Name the blood parasite species.
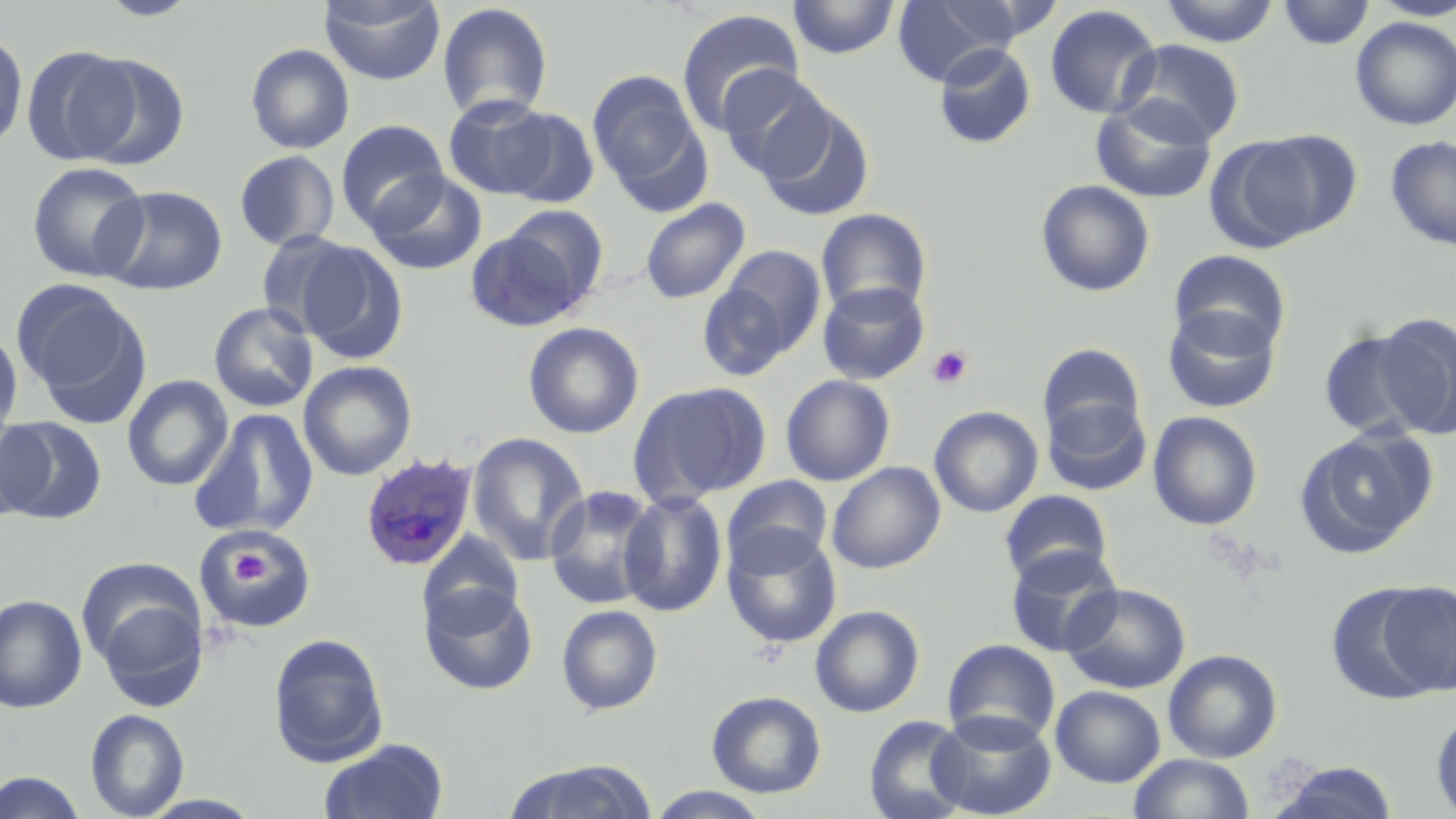

Plasmodium ovale.

Approximate bounding boxes as (x1, y1, x2, y2) in pixels. Platelet locations: (927, 345, 973, 389), (223, 540, 276, 591). Uninfected red blood cell locations: (96, 0, 203, 20), (319, 0, 445, 85), (787, 0, 900, 59), (890, 0, 1019, 87), (1156, 0, 1281, 46), (1275, 0, 1375, 50), (1370, 1, 1456, 21), (436, 2, 554, 122), (1044, 4, 1162, 120), (676, 7, 804, 135), (1351, 16, 1456, 130), (0, 31, 27, 155), (1117, 40, 1245, 145), (933, 42, 1036, 148), (245, 43, 354, 154), (22, 45, 140, 166), (72, 54, 190, 170), (717, 65, 832, 180), (588, 70, 708, 206), (442, 94, 560, 199), (1091, 96, 1217, 203), (757, 101, 874, 222), (498, 108, 599, 208), (336, 119, 449, 233), (1241, 130, 1363, 241), (1385, 134, 1456, 250), (234, 151, 340, 251), (26, 161, 150, 282), (366, 171, 487, 276), (1036, 179, 1156, 297), (98, 185, 228, 295), (640, 198, 751, 304), (500, 204, 610, 310), (815, 208, 932, 316), (465, 228, 588, 332), (254, 230, 358, 338), (297, 241, 409, 363), (716, 245, 826, 359), (1169, 249, 1292, 357), (817, 282, 930, 385), (15, 283, 150, 425), (697, 284, 794, 381), (208, 302, 319, 413), (1163, 306, 1281, 414), (1375, 314, 1456, 439), (523, 321, 644, 439), (0, 327, 23, 447), (1317, 328, 1433, 441), (1037, 343, 1146, 443), (299, 360, 417, 480), (123, 375, 233, 491), (780, 375, 895, 486), (629, 380, 773, 506), (1042, 399, 1151, 496), (929, 406, 1043, 517), (190, 409, 319, 538), (1147, 411, 1263, 530), (0, 416, 107, 524), (0, 417, 48, 524), (1294, 426, 1438, 558), (466, 431, 590, 565), (827, 461, 945, 573), (722, 475, 833, 574), (545, 485, 660, 610), (999, 490, 1113, 586), (619, 491, 727, 617), (194, 524, 317, 633), (722, 527, 842, 649), (418, 531, 524, 634), (1005, 546, 1123, 657), (1375, 581, 1456, 697), (419, 583, 539, 695), (1061, 583, 1191, 694), (89, 584, 210, 712), (0, 594, 87, 713), (556, 604, 662, 715), (810, 605, 925, 717), (268, 633, 389, 767), (943, 639, 1060, 748), (1163, 649, 1282, 763), (1051, 685, 1165, 787), (707, 690, 827, 798), (85, 708, 189, 818), (1431, 709, 1456, 817), (929, 711, 1057, 819), (864, 715, 972, 819), (319, 737, 449, 819), (1129, 753, 1254, 819), (503, 758, 659, 819), (1265, 761, 1402, 819), (0, 771, 88, 818), (645, 787, 774, 819). Plasmodium ovale-infected red blood cell locations: (359, 452, 479, 571). Captured at 1000x magnification. May-Grünwald-Giemsa-stained preparation. Single field of view. Thin blood film. Optical microscopy. Image is 1456×819 pixels.